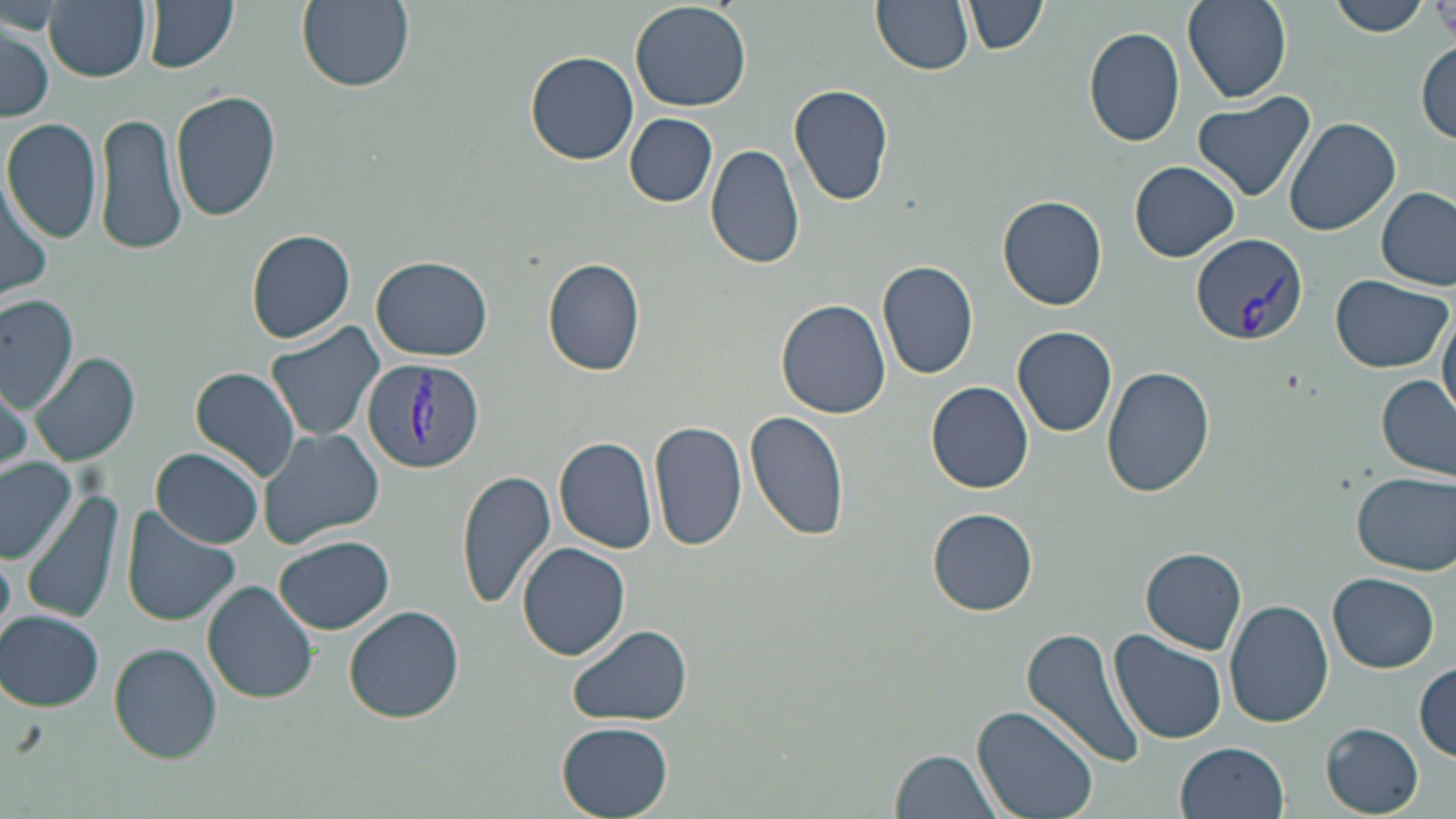

Approximate bounding boxes as named x1/y1/x2/y2 corners in pixels. Uninfected red blood cell locations: (x1=140, y1=0, x2=240, y2=73), (x1=296, y1=0, x2=415, y2=91), (x1=631, y1=0, x2=752, y2=112), (x1=874, y1=0, x2=974, y2=76), (x1=965, y1=0, x2=1047, y2=56), (x1=1183, y1=0, x2=1291, y2=104), (x1=1328, y1=0, x2=1431, y2=38), (x1=42, y1=1, x2=151, y2=80), (x1=1433, y1=1, x2=1456, y2=44), (x1=0, y1=19, x2=55, y2=121), (x1=1083, y1=26, x2=1186, y2=148), (x1=1415, y1=41, x2=1454, y2=146), (x1=524, y1=51, x2=640, y2=166), (x1=789, y1=83, x2=895, y2=207), (x1=1190, y1=90, x2=1314, y2=203), (x1=171, y1=92, x2=282, y2=225), (x1=93, y1=110, x2=187, y2=257), (x1=625, y1=113, x2=717, y2=207), (x1=2, y1=116, x2=104, y2=246), (x1=1283, y1=116, x2=1400, y2=237), (x1=705, y1=143, x2=808, y2=269), (x1=1130, y1=161, x2=1239, y2=261), (x1=0, y1=177, x2=55, y2=304), (x1=1376, y1=187, x2=1454, y2=289), (x1=996, y1=194, x2=1109, y2=311), (x1=246, y1=228, x2=357, y2=345), (x1=373, y1=255, x2=493, y2=361), (x1=542, y1=257, x2=647, y2=378), (x1=877, y1=261, x2=979, y2=379), (x1=1329, y1=275, x2=1451, y2=374), (x1=1351, y1=279, x2=1450, y2=471), (x1=0, y1=295, x2=78, y2=411), (x1=777, y1=299, x2=892, y2=419), (x1=1438, y1=302, x2=1456, y2=420), (x1=264, y1=321, x2=387, y2=444), (x1=1013, y1=325, x2=1118, y2=436), (x1=30, y1=352, x2=140, y2=468), (x1=191, y1=366, x2=301, y2=482), (x1=1101, y1=366, x2=1214, y2=499), (x1=1377, y1=374, x2=1455, y2=479), (x1=0, y1=375, x2=31, y2=472), (x1=926, y1=381, x2=1032, y2=494), (x1=745, y1=408, x2=849, y2=542), (x1=649, y1=418, x2=748, y2=554), (x1=256, y1=427, x2=386, y2=550), (x1=554, y1=436, x2=659, y2=553), (x1=153, y1=448, x2=263, y2=547), (x1=0, y1=458, x2=78, y2=562), (x1=456, y1=467, x2=557, y2=610), (x1=1353, y1=472, x2=1455, y2=575), (x1=23, y1=489, x2=126, y2=626), (x1=926, y1=507, x2=1040, y2=616), (x1=121, y1=510, x2=240, y2=626), (x1=275, y1=535, x2=395, y2=635), (x1=517, y1=542, x2=629, y2=659), (x1=1142, y1=547, x2=1247, y2=653), (x1=1327, y1=571, x2=1441, y2=673), (x1=203, y1=580, x2=318, y2=704), (x1=1225, y1=599, x2=1334, y2=730), (x1=343, y1=606, x2=463, y2=725), (x1=2, y1=610, x2=105, y2=712), (x1=567, y1=624, x2=693, y2=727), (x1=1022, y1=625, x2=1150, y2=771), (x1=1110, y1=631, x2=1228, y2=744), (x1=111, y1=643, x2=223, y2=763), (x1=1415, y1=663, x2=1455, y2=760), (x1=973, y1=704, x2=1100, y2=819), (x1=556, y1=721, x2=673, y2=817), (x1=1320, y1=724, x2=1425, y2=815), (x1=1177, y1=741, x2=1290, y2=819), (x1=891, y1=750, x2=1005, y2=819). Plasmodium vivax-infected red blood cell locations: (x1=1191, y1=232, x2=1307, y2=349), (x1=361, y1=357, x2=485, y2=473). Slide-level diagnosis: Plasmodium vivax. Image is 1456×819 pixels. One field of a larger specimen. 1000x magnification. Thin blood smear. Light microscopy. May-Grünwald-Giemsa-stained preparation.